Report the malaria status of this cell.
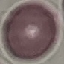
Uninfected.

Cell patch, automatically extracted from a larger field of view and resized to 64 × 64 pixels. Acquired by smartphone through the microscope eyepiece. Thin smear of blood. Giemsa stain.